Give the position of every Plasmodium parasite.
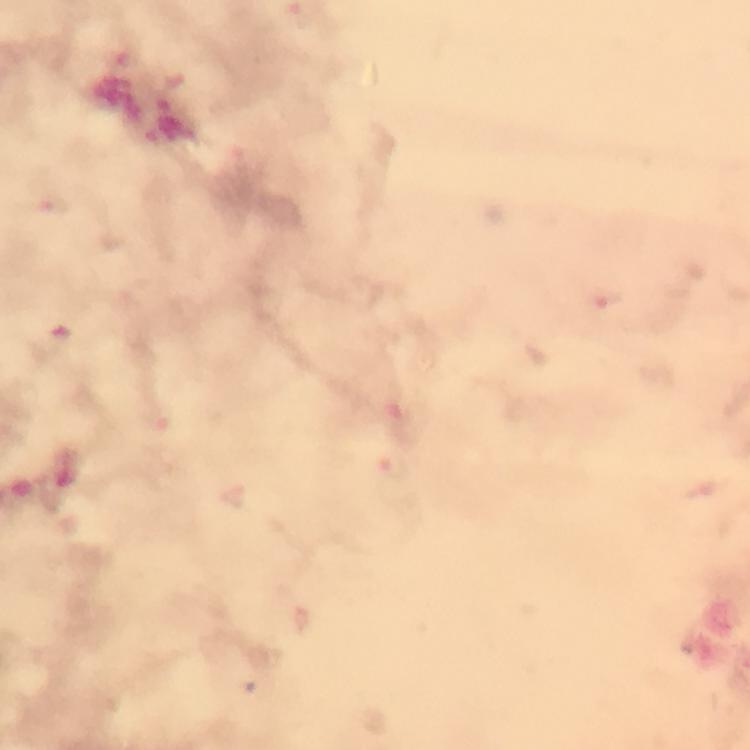
Approximate centers as [x, y] in pixels.
Plasmodium parasites: [394, 468].

Summary:
  - Stain: Giemsa
  - Capture: smartphone mounted on the microscope
  - Preparation: thick blood smear
  - Context: from a malaria diagnostic workup
  - Immersion oil: used
  - Magnification: 100x
  - Cropped from: a single field of view
  - Image size: 750×750 pixels